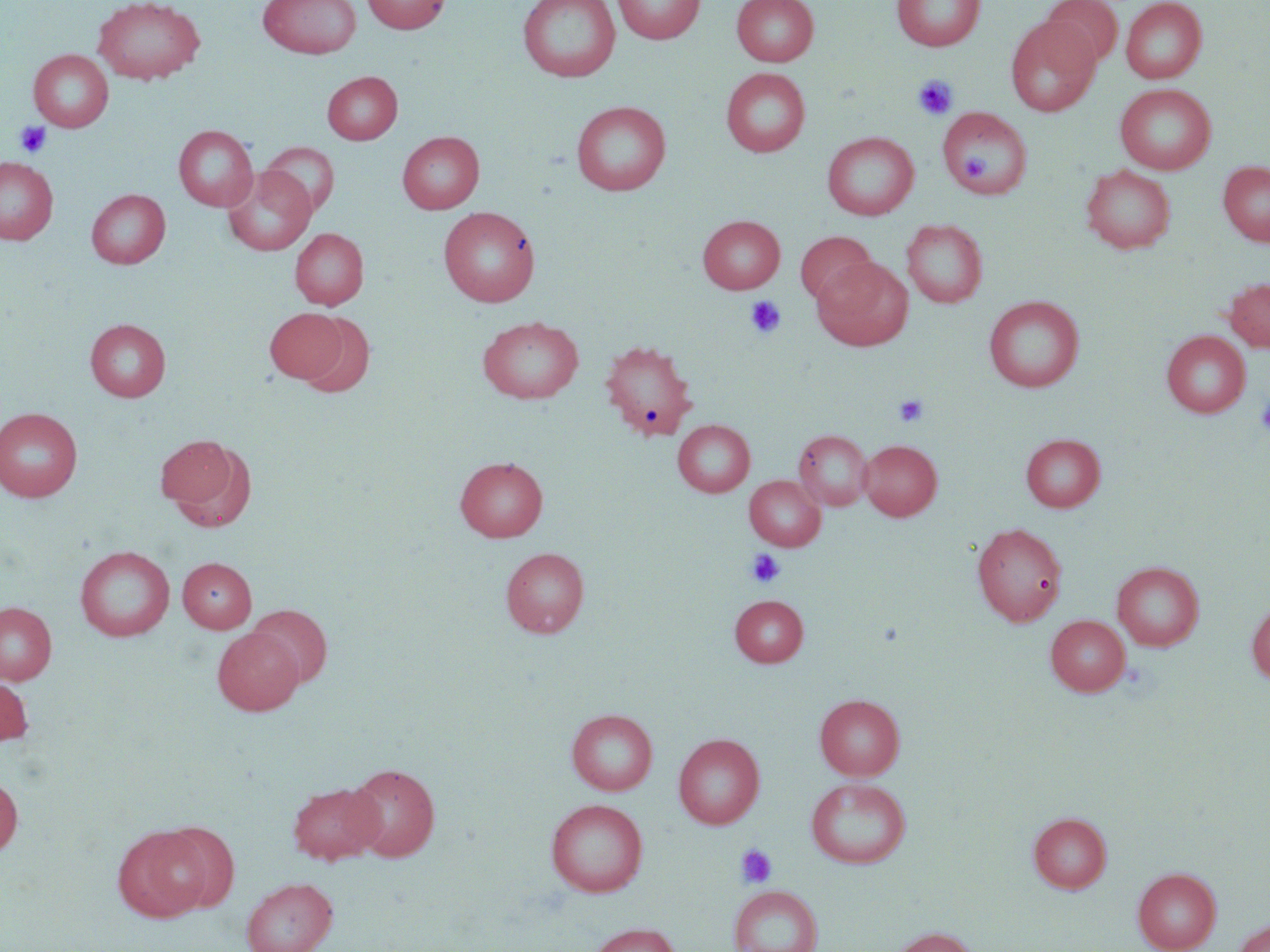 Approximate bounding boxes as (x1,y1)-(x2,y2) corner pairs in pixels. Uninfected red blood cell locations: (92,0)-(206,85), (258,0)-(361,59), (361,0)-(450,34), (517,0)-(621,82), (612,0)-(705,44), (731,0)-(819,66), (892,0)-(985,51), (1043,0)-(1123,68), (1121,0)-(1207,84), (1005,17)-(1101,117), (28,49)-(113,132), (720,68)-(810,157), (323,71)-(401,144), (1115,84)-(1216,175), (571,100)-(672,195), (937,107)-(1032,198), (173,125)-(258,211), (397,131)-(484,213), (822,131)-(919,220), (259,141)-(339,217), (0,157)-(58,245), (1218,161)-(1270,246), (1082,164)-(1176,254), (222,166)-(316,256), (86,189)-(170,268), (438,206)-(540,307), (698,215)-(785,294), (901,219)-(988,308), (290,228)-(368,309), (795,231)-(876,307), (812,256)-(913,350), (1223,278)-(1270,352), (984,296)-(1085,392), (265,307)-(347,383), (297,312)-(376,399), (477,316)-(584,404), (85,318)-(171,401), (1161,330)-(1251,418), (600,338)-(699,439), (0,407)-(83,502), (673,419)-(755,497), (793,429)-(873,511), (155,433)-(249,522), (1021,433)-(1105,512), (859,439)-(942,521), (455,456)-(548,542), (744,476)-(825,551), (971,522)-(1068,626), (74,545)-(175,641), (501,547)-(588,638), (178,558)-(256,633), (1112,561)-(1204,651), (730,595)-(808,667), (0,601)-(56,684), (1247,601)-(1270,685), (246,604)-(333,689), (1045,614)-(1130,695), (212,629)-(303,715), (0,675)-(33,746), (815,694)-(905,780), (566,708)-(657,795), (563,710)-(655,893), (673,733)-(765,829), (345,762)-(440,862), (0,774)-(23,858), (807,778)-(910,868), (288,780)-(382,864), (546,798)-(648,896), (1028,812)-(1112,893), (157,821)-(239,912), (112,826)-(210,922), (1133,867)-(1221,952), (241,877)-(338,952), (729,885)-(823,952), (1234,919)-(1270,952), (588,922)-(681,952), (889,926)-(980,952). Platelet locations: (913,75)-(958,120), (15,121)-(52,158), (744,295)-(786,340), (893,394)-(929,427), (1255,395)-(1270,438), (746,549)-(785,587), (736,844)-(777,888). Slide-level diagnosis: negative for blood parasites. Thin blood film. May-Grünwald-Giemsa-stained preparation. Image is 1270×952 pixels. 1000x magnification. Single field of view. Light microscopy.